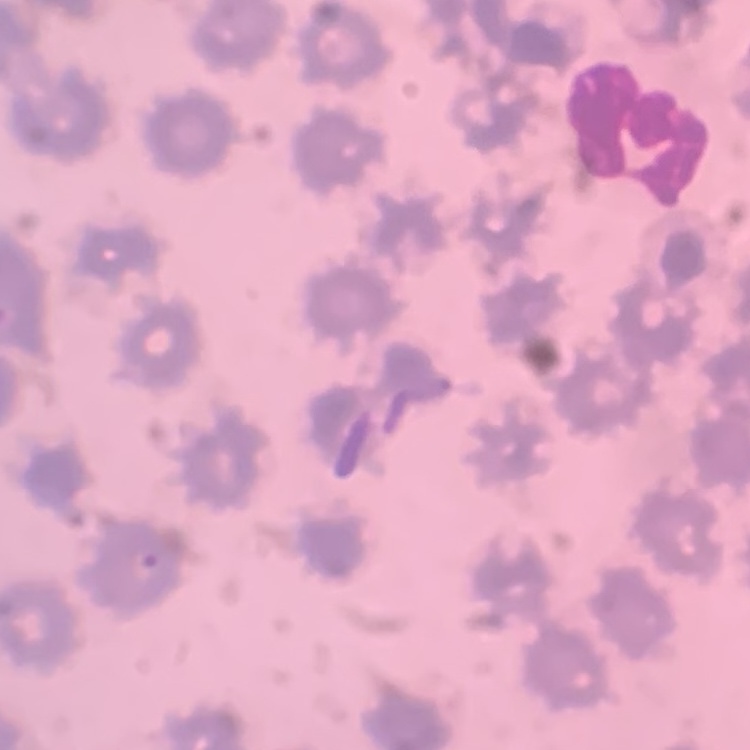

Summary:
  - Red blood cell morphology: no rouleaux formation
  - Stain: Field's or Giemsa
  - Image type: one tile cut from a larger photomicrograph
  - Preparation: thin blood film